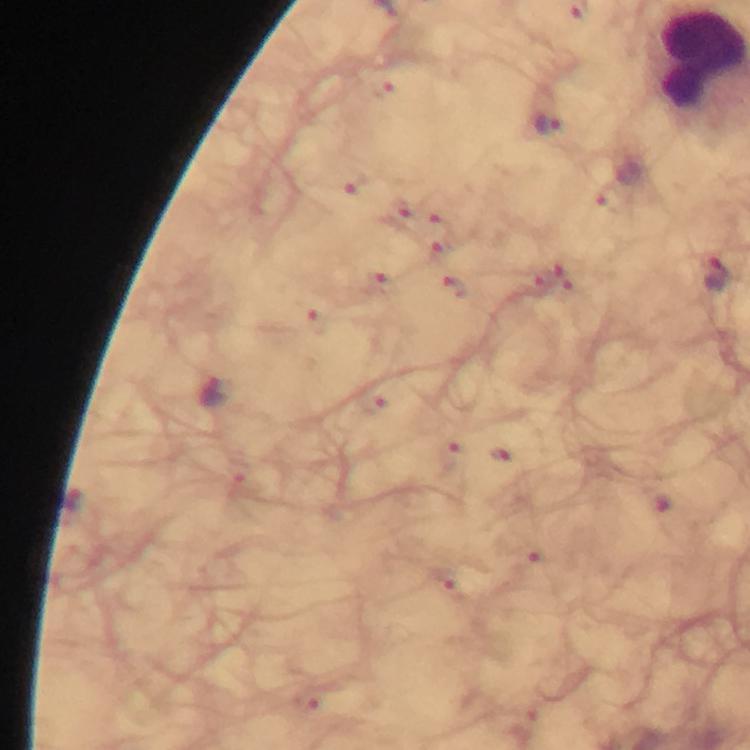

{
  "magnification": "100x",
  "image_size": "750×750 pixels",
  "preparation": "thick blood smear",
  "cropped_from": "a single field of view",
  "plasmodium_parasite_locations": "approximate centers as (x, y) in pixels: (547, 125), (355, 185), (608, 199), (399, 215), (440, 225), (438, 254), (714, 275), (380, 284), (456, 291), (316, 322), (213, 396), (372, 404), (449, 457), (664, 504), (447, 584)",
  "stain": "Giemsa",
  "context": "from a diagnostic examination for malaria",
  "immersion_oil": "applied",
  "capture": "smartphone camera through the microscope"
}